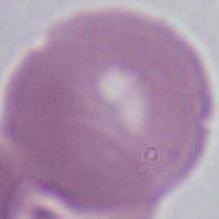

{
  "identification": "erythrocyte",
  "modality": "photomicrograph",
  "magnification": "1000x"
}